Give the extent of all Plasmodium falciparum-infected red blood cells.
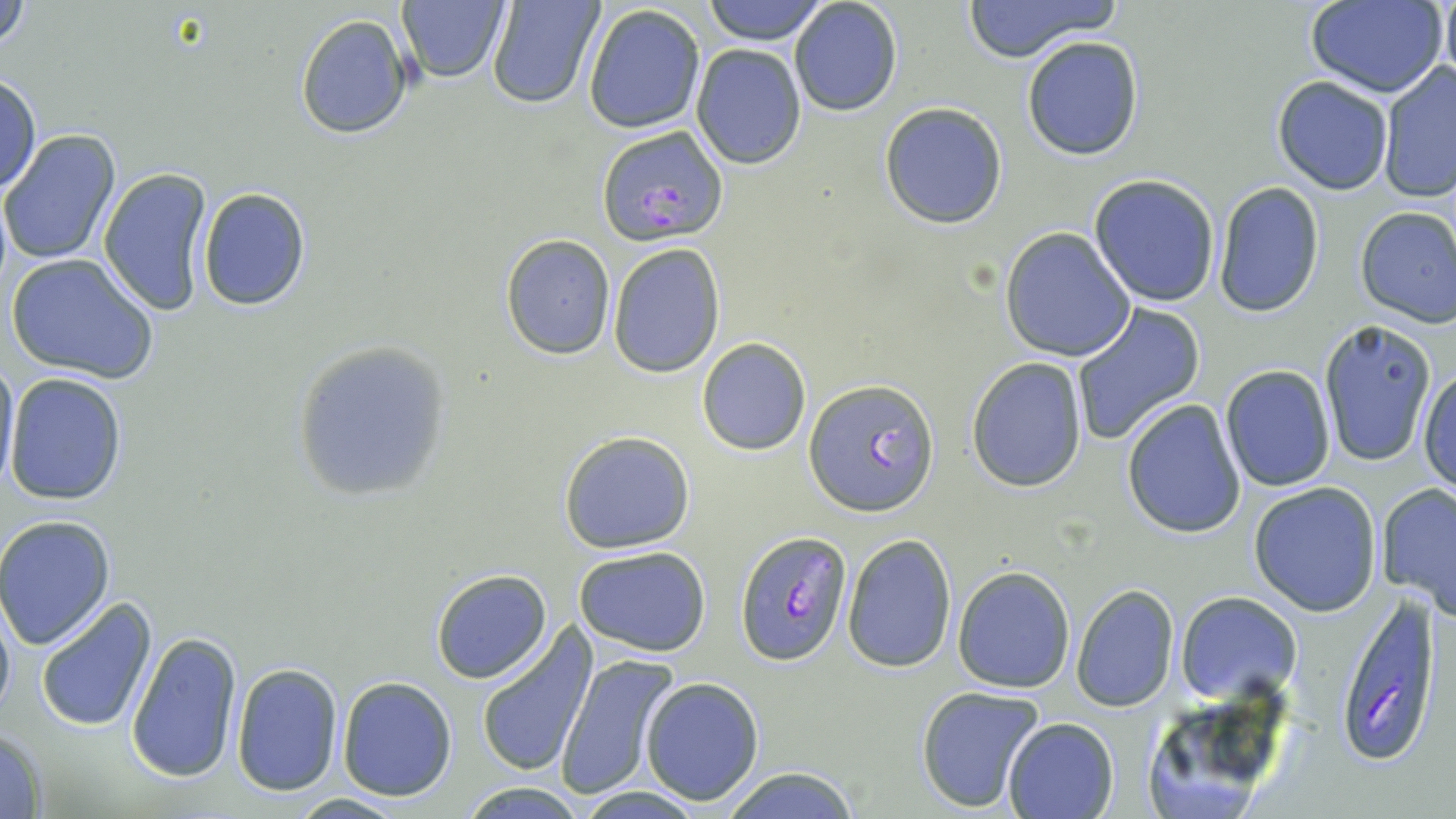

Approximate bounding boxes as (x1,y1)-(x2,y2) corner pairs in pixels.
Plasmodium falciparum-infected red blood cells: (596,125)-(728,246), (805,380)-(940,515), (735,531)-(851,665), (1331,589)-(1446,769).

slide-level diagnosis = Plasmodium falciparum
stain = May-Grünwald-Giemsa
uninfected red blood cell locations = approximate bounding boxes as (x1,y1)-(x2,y2) corner pairs in pixels: (2,0)-(30,58), (703,0)-(829,44), (788,0)-(901,117), (960,0)-(1122,61), (1303,0)-(1449,98), (1439,0)-(1456,89), (485,1)-(606,110), (395,2)-(511,83), (583,5)-(707,133), (294,14)-(415,139), (1022,36)-(1145,159), (691,44)-(808,169), (1377,61)-(1456,202), (1,72)-(41,195), (1273,76)-(1396,195), (879,101)-(1008,229), (1,130)-(122,266), (97,165)-(216,316), (1088,173)-(1221,307), (1214,182)-(1324,318), (198,187)-(310,311), (1355,205)-(1456,327), (1000,226)-(1137,362), (501,236)-(615,358), (607,242)-(725,378), (7,253)-(159,384), (1069,304)-(1206,446), (1311,322)-(1436,466), (696,337)-(813,456), (290,340)-(454,506), (1,354)-(20,491), (965,357)-(1088,491), (1220,364)-(1336,493), (1418,369)-(1455,497), (4,372)-(127,505), (1121,399)-(1248,540), (557,429)-(697,553), (1375,481)-(1456,614), (1248,482)-(1383,617), (1,516)-(118,651), (842,534)-(957,673), (573,545)-(712,657), (952,565)-(1076,693), (430,569)-(552,684), (1070,584)-(1180,712), (1175,592)-(1300,703), (0,595)-(16,726), (35,596)-(159,733), (475,626)-(597,777), (125,631)-(244,784), (554,655)-(678,800), (230,663)-(343,795), (336,675)-(457,801), (640,676)-(765,805), (915,685)-(1047,815), (1133,690)-(1298,816), (1003,717)-(1120,819), (0,728)-(50,817), (715,766)-(860,819), (456,783)-(589,817), (570,786)-(709,818), (289,792)-(410,818)
magnification = 1000x
preparation = thin blood film
image size = 1456×819 pixels
modality = light microscopy
field of view = single